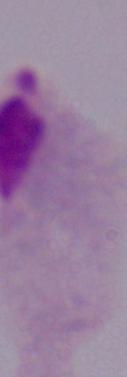

Summary:
  - Magnification: 1000x
  - Modality: photomicrograph
  - Identification: trichomonad